Classify this cell by malaria status.
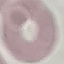

Uninfected.

Summary:
  - Image type: automatically extracted cell patch, resized to 64 × 64 pixels
  - Stain: Giemsa
  - Capture: smartphone camera at the microscope eyepiece
  - Preparation: thin blood smear